Comment on the morphology of the red blood cells.
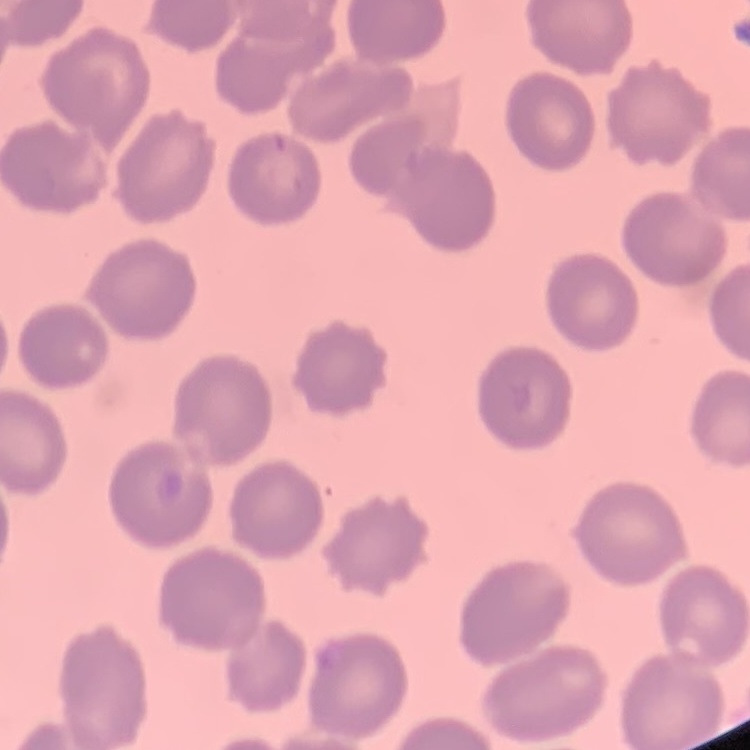
No rouleaux formation.

Summary:
  - Stain: Field's or Giemsa
  - Preparation: thin peripheral smear
  - Image type: square crop of a larger photomicrograph